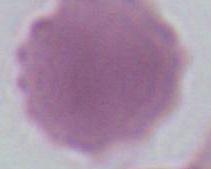

modality: micrograph
identification: erythrocyte
magnification: 1000x